Identify the blood parasite species.
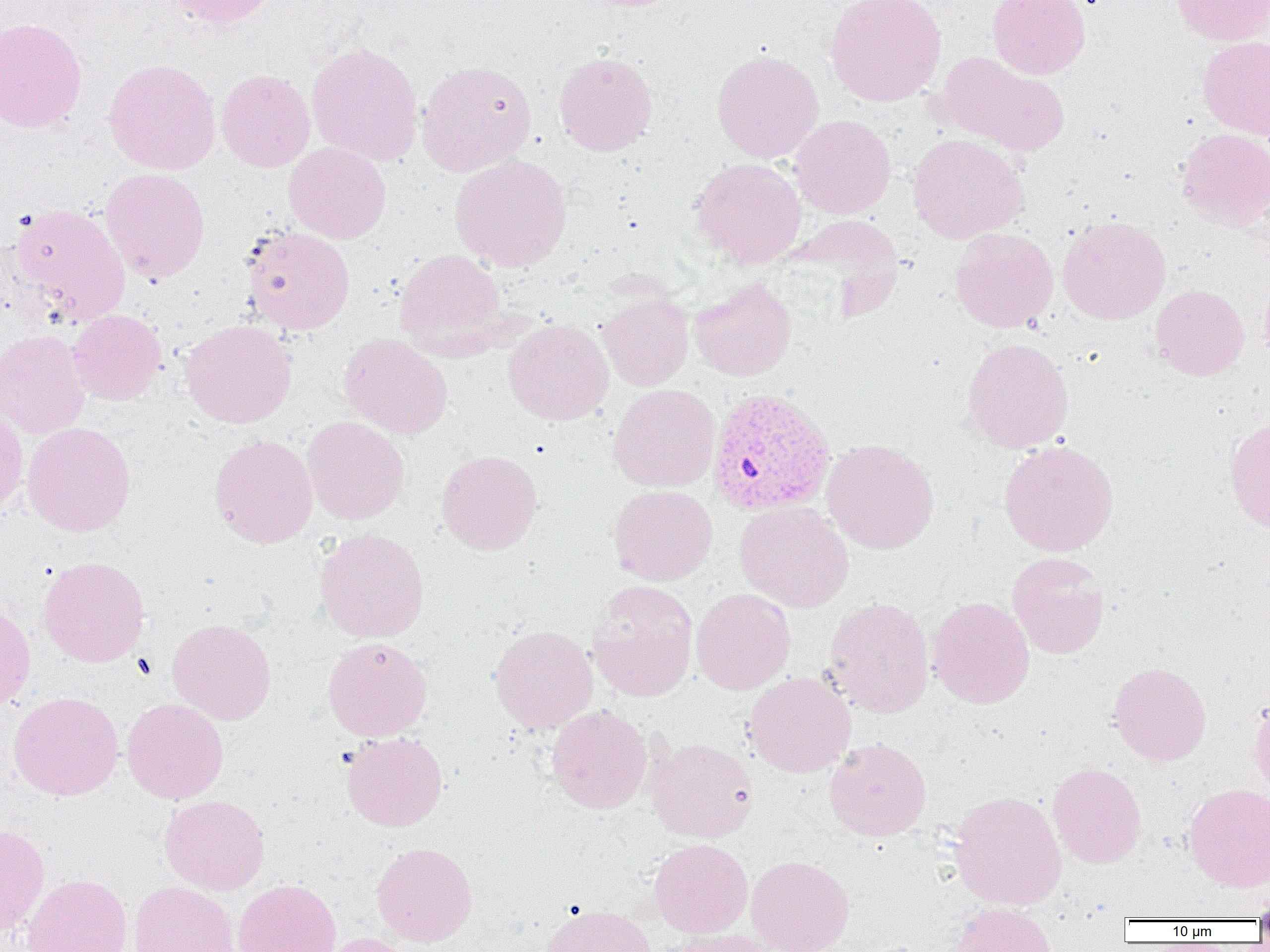

Plasmodium vivax.

Approximate bounding boxes as (x1,y1)-(x2,y2) corner pairs in pixels. Plasmodium vivax-infected red blood cell locations: (707,387)-(836,517). Uninfected red blood cell locations: (164,0)-(282,29), (825,0)-(946,106), (987,0)-(1090,79), (1171,0)-(1270,45), (0,17)-(88,133), (1197,36)-(1270,140), (306,41)-(423,166), (711,49)-(824,163), (553,51)-(658,156), (937,52)-(1070,156), (103,58)-(221,175), (416,59)-(537,176), (216,69)-(316,172), (790,115)-(896,219), (1176,128)-(1270,230), (907,133)-(1028,243), (283,142)-(391,243), (450,154)-(572,271), (690,157)-(806,267), (100,167)-(210,283), (10,202)-(130,325), (783,215)-(905,318), (1057,216)-(1171,325), (241,226)-(356,334), (950,227)-(1058,332), (394,249)-(509,356), (1258,272)-(1270,371), (689,278)-(796,381), (1150,285)-(1249,381), (598,293)-(694,391), (68,310)-(166,405), (180,319)-(297,428), (503,319)-(614,425), (0,330)-(91,439), (339,333)-(453,439), (962,337)-(1074,453), (608,384)-(720,492), (0,406)-(28,516), (1224,415)-(1270,534), (302,416)-(409,525), (22,421)-(136,536), (209,434)-(318,548), (821,439)-(939,554), (999,439)-(1119,557), (436,449)-(542,554), (608,484)-(718,586), (735,501)-(854,612), (314,527)-(429,644), (1007,552)-(1109,659), (38,555)-(150,667), (586,580)-(699,702), (691,588)-(795,695), (824,596)-(934,718), (927,596)-(1035,709), (0,602)-(35,711), (167,617)-(277,725), (489,625)-(598,734), (322,637)-(432,741), (1107,662)-(1212,765), (744,672)-(856,777), (8,691)-(123,800), (1249,692)-(1270,800), (122,698)-(229,804), (546,704)-(653,814), (341,731)-(447,832), (646,737)-(758,842), (824,737)-(932,840), (1048,762)-(1146,868), (1183,783)-(1270,891), (949,790)-(1067,910), (159,795)-(270,895), (0,823)-(50,936), (649,838)-(753,937), (371,841)-(477,947), (746,855)-(854,952), (21,874)-(132,952), (233,879)-(342,952), (129,881)-(240,952), (1252,887)-(1270,926), (540,902)-(658,952), (949,902)-(1057,952), (658,928)-(783,952), (318,933)-(416,952). Optical microscopy. Thin blood smear. Image is 1270×952 pixels. Single field of view. 1000x magnification.